Assess the morphology of the red blood cells.
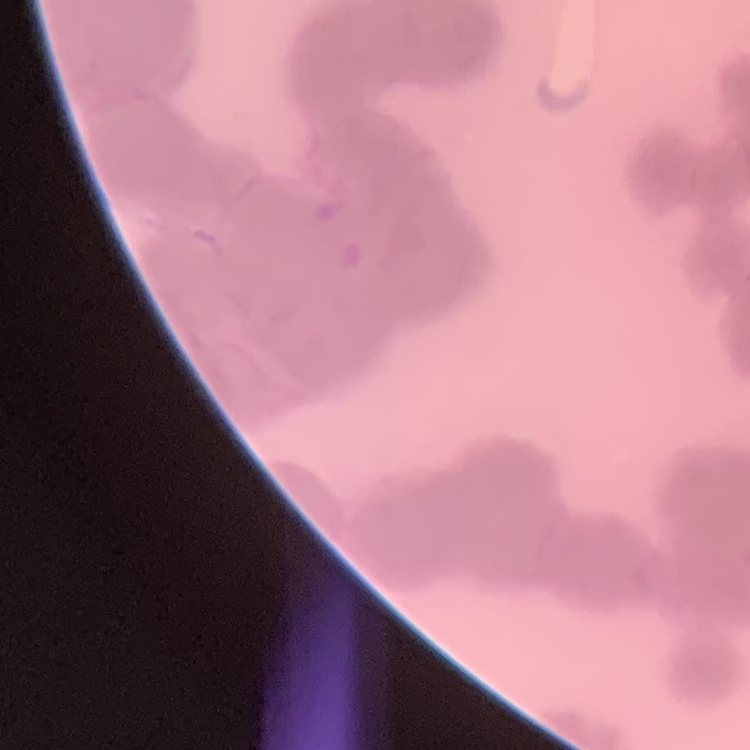
They show rouleaux formation.

One tile cut from a larger photomicrograph. Field's or Giemsa stain. Thin blood smear.